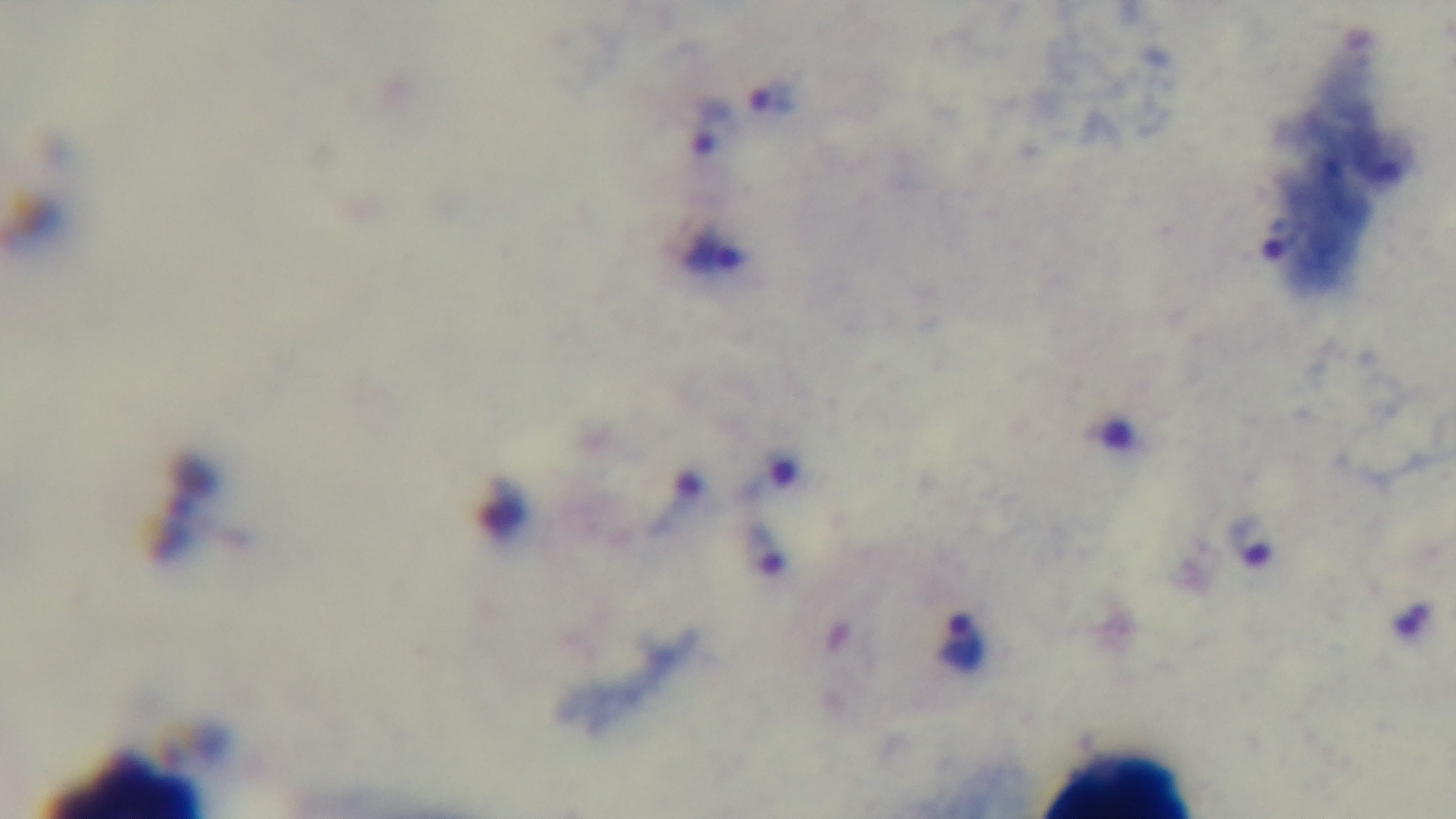
Summary:
  - Malaria status: positive
  - Capture: mounted 4K digital camera
  - Objective: 100x oil immersion
  - Modality: light microscopy
  - Preparation: thick smear
  - Stain: Giemsa
  - Field of view: one from the slide